Name the parasite shown.
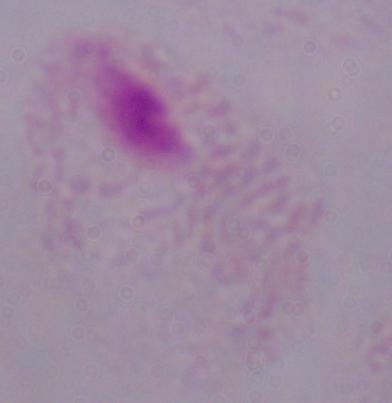

A trichomonad.

Summary:
  - Magnification: 1000x
  - Modality: photomicrograph